Point out each leukocyte.
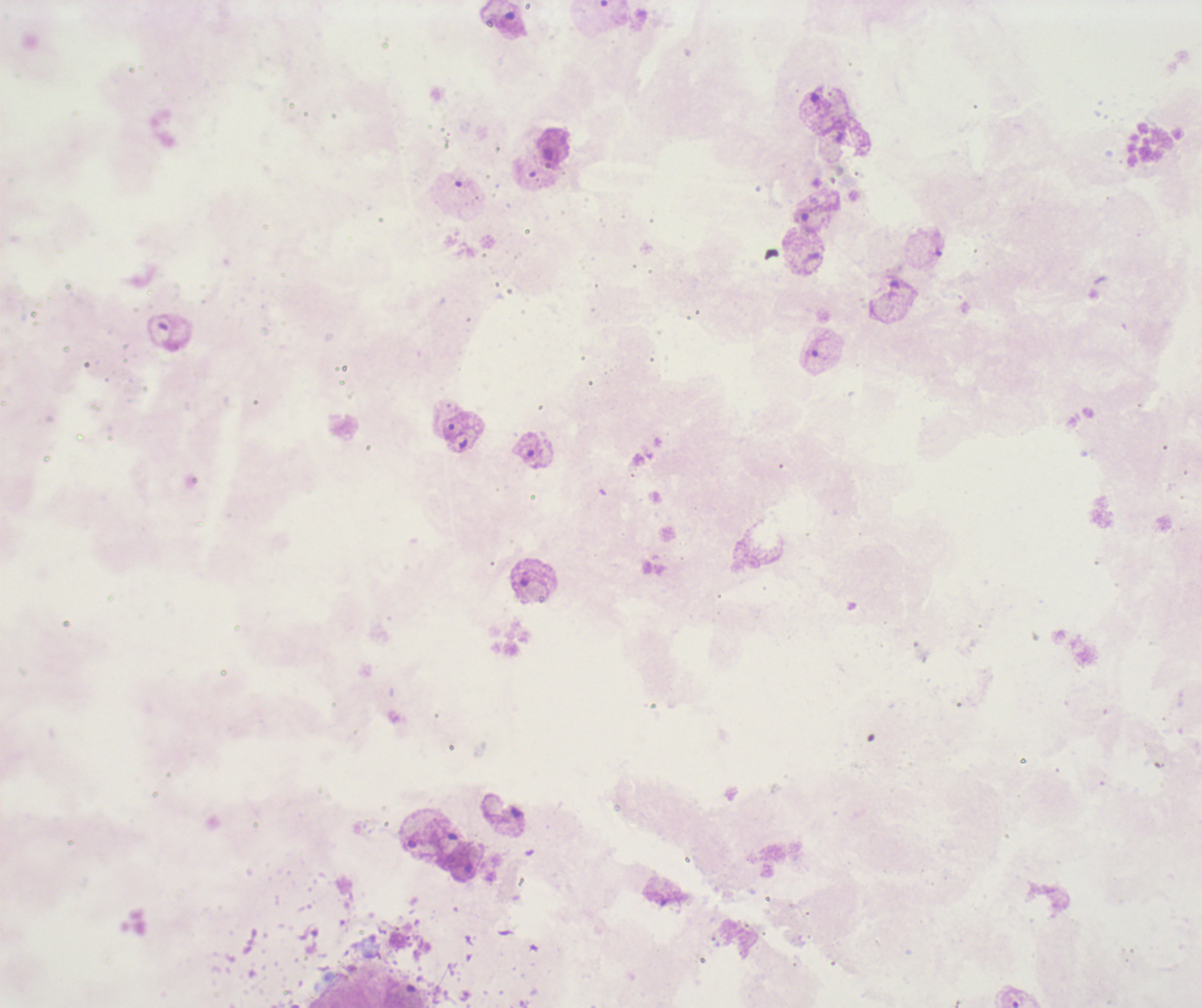
No leukocytes visible.

coordinate format = approximate centers as {x, y} in pixels
trophozoite locations = {454, 431}
image size = 1202×1008 pixels
context = previously used in an actual diagnosis
preparation = thick blood smear
coloration quality = bad
stain = Romanowsky
result = positive for Plasmodium parasites
background quality = poor
magnification = 100x
field of view = single